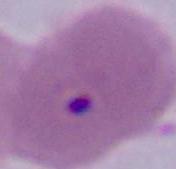
modality = micrograph
identification = Plasmodium
magnification = 400x or 1000x